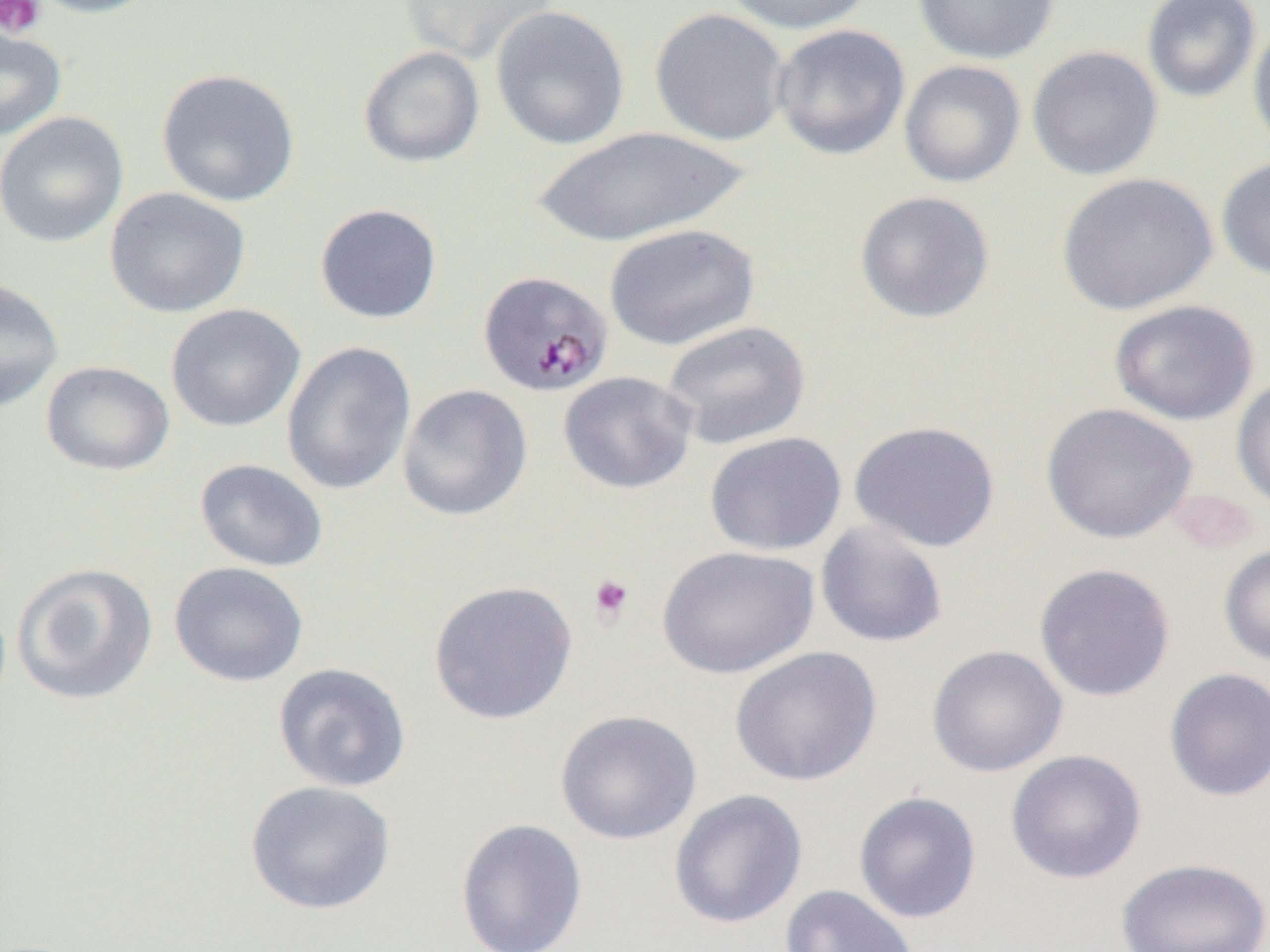

Approximate bounding boxes as named x1/y1/x2/y2 corners in pixels. Plasmodium malariae-infected red blood cell locations: (x1=477, y1=270, x2=613, y2=396). Uninfected red blood cell locations: (x1=26, y1=0, x2=163, y2=18), (x1=399, y1=0, x2=558, y2=66), (x1=722, y1=0, x2=876, y2=34), (x1=912, y1=0, x2=1059, y2=64), (x1=1141, y1=0, x2=1261, y2=103), (x1=490, y1=5, x2=629, y2=150), (x1=650, y1=7, x2=790, y2=146), (x1=1248, y1=20, x2=1270, y2=160), (x1=771, y1=23, x2=911, y2=160), (x1=0, y1=24, x2=67, y2=143), (x1=358, y1=45, x2=485, y2=168), (x1=1026, y1=45, x2=1163, y2=181), (x1=899, y1=59, x2=1026, y2=188), (x1=155, y1=68, x2=300, y2=207), (x1=0, y1=111, x2=129, y2=248), (x1=530, y1=125, x2=752, y2=248), (x1=1216, y1=156, x2=1270, y2=280), (x1=1056, y1=172, x2=1219, y2=315), (x1=105, y1=187, x2=250, y2=318), (x1=854, y1=190, x2=995, y2=323), (x1=314, y1=203, x2=442, y2=324), (x1=604, y1=222, x2=760, y2=350), (x1=0, y1=275, x2=63, y2=413), (x1=1109, y1=298, x2=1260, y2=426), (x1=165, y1=303, x2=305, y2=432), (x1=661, y1=319, x2=812, y2=450), (x1=281, y1=341, x2=417, y2=495), (x1=40, y1=360, x2=175, y2=476), (x1=558, y1=370, x2=698, y2=494), (x1=1231, y1=373, x2=1270, y2=514), (x1=397, y1=384, x2=533, y2=521), (x1=1040, y1=402, x2=1198, y2=544), (x1=849, y1=419, x2=1002, y2=553), (x1=704, y1=431, x2=847, y2=556), (x1=195, y1=458, x2=329, y2=572), (x1=815, y1=520, x2=949, y2=647), (x1=1219, y1=543, x2=1270, y2=667), (x1=656, y1=545, x2=819, y2=679), (x1=169, y1=561, x2=309, y2=687), (x1=12, y1=562, x2=158, y2=705), (x1=1034, y1=562, x2=1176, y2=701), (x1=427, y1=580, x2=579, y2=725), (x1=926, y1=644, x2=1068, y2=778), (x1=728, y1=645, x2=882, y2=787), (x1=273, y1=662, x2=411, y2=793), (x1=1163, y1=667, x2=1270, y2=802), (x1=555, y1=709, x2=702, y2=844), (x1=1005, y1=749, x2=1146, y2=884), (x1=245, y1=780, x2=397, y2=915), (x1=668, y1=788, x2=808, y2=929), (x1=853, y1=790, x2=982, y2=924), (x1=455, y1=817, x2=588, y2=952), (x1=1115, y1=857, x2=1270, y2=952), (x1=780, y1=885, x2=920, y2=952). Platelet locations: (x1=0, y1=0, x2=45, y2=38), (x1=587, y1=574, x2=635, y2=625). Slide-level diagnosis: Plasmodium malariae. Image is 1270×952 pixels. Single field of view. Optical microscopy. 1000x magnification. Thin blood smear.